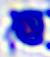
identification: white blood cell
modality: photomicrograph
magnification: 400x